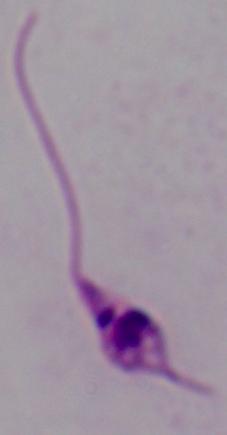
Micrograph. 1000x magnification. A Leishmania parasite is shown.